Classify this cell by malaria status.
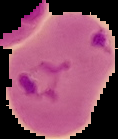

Parasitized.

Summary:
  - Preparation: thin blood film
  - Image type: segmented cell region on a black background
  - Image size: 118×139 pixels